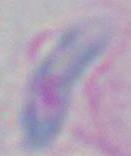
identification = Toxoplasma gondii
magnification = 1000x
modality = photomicrograph